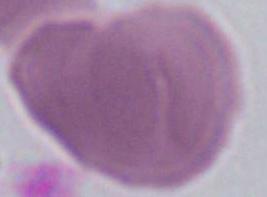

{
  "identification": "red blood cell",
  "magnification": "1000x",
  "modality": "photomicrograph"
}